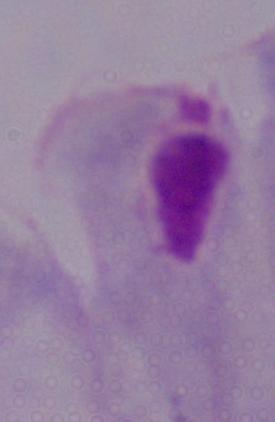
A trichomonad is shown. Photomicrograph. Captured at 1000x magnification.